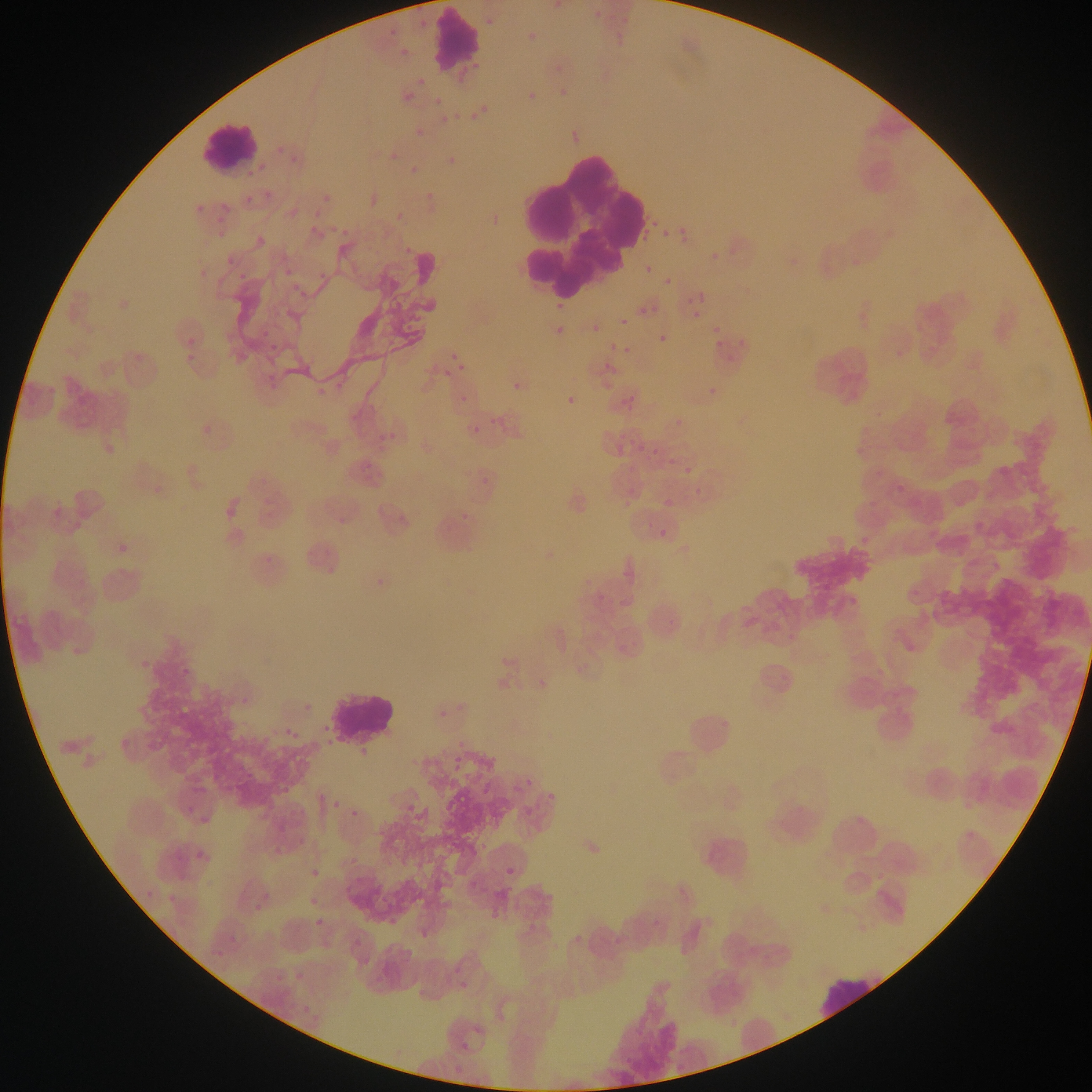

Approximate bounding boxes as [left, top, right, bottom] in pixels.
Summary:
  - Leukocyte locations: [436, 12, 479, 67], [201, 125, 258, 171], [514, 153, 644, 291], [321, 686, 400, 750], [818, 971, 889, 1016]
  - Plasmodium parasite locations (subset; some below the resolvable size): [410, 15, 429, 27], [485, 18, 493, 26], [384, 29, 392, 38], [395, 42, 410, 56], [452, 68, 473, 87], [416, 73, 427, 90], [399, 91, 418, 106], [471, 93, 489, 119], [434, 96, 443, 106], [435, 110, 460, 126], [383, 149, 400, 167], [287, 150, 302, 164], [441, 150, 466, 164], [409, 158, 423, 179], [268, 183, 289, 199], [202, 186, 226, 218], [359, 189, 378, 208], [242, 190, 258, 209], [424, 192, 440, 204], [288, 198, 309, 217], [394, 205, 410, 221], [644, 209, 660, 241], [304, 219, 318, 238], [331, 220, 352, 237], [681, 225, 694, 244], [260, 227, 273, 238], [319, 253, 339, 279], [224, 255, 237, 265], [645, 265, 653, 274], [236, 267, 257, 287], [284, 278, 307, 306], [663, 278, 671, 287], [682, 292, 704, 307], [550, 299, 570, 315], [648, 306, 665, 312], [638, 307, 647, 315], [693, 311, 701, 319], [620, 318, 628, 326], [551, 321, 571, 334], [587, 323, 601, 338], [253, 326, 282, 349], [713, 326, 721, 333], [658, 334, 667, 342], [187, 336, 196, 346], [605, 338, 622, 355], [445, 347, 474, 378], [604, 363, 612, 372], [444, 369, 452, 377], [510, 383, 524, 391], [563, 390, 580, 404], [614, 391, 638, 408], [457, 393, 467, 402], [487, 406, 501, 431], [196, 414, 217, 440], [102, 421, 130, 455], [470, 425, 480, 434], [625, 441, 635, 451], [638, 444, 644, 461], [652, 448, 660, 456], [667, 459, 676, 467], [685, 467, 693, 474], [481, 477, 489, 485], [895, 484, 906, 494], [664, 498, 674, 507], [623, 499, 631, 508], [219, 506, 246, 520], [337, 517, 346, 526], [974, 521, 983, 530], [658, 528, 666, 536], [855, 530, 871, 544], [110, 540, 132, 557], [993, 562, 1001, 571], [374, 579, 388, 586], [134, 651, 149, 670], [180, 653, 193, 676], [532, 678, 544, 690], [236, 687, 252, 707], [282, 709, 305, 740], [437, 710, 451, 722], [1041, 714, 1049, 722], [447, 747, 468, 777], [522, 772, 534, 786], [192, 775, 211, 799], [970, 775, 978, 784], [475, 781, 492, 799], [544, 781, 560, 811], [312, 786, 331, 803], [180, 793, 196, 815], [327, 795, 344, 814], [195, 799, 218, 826], [516, 801, 538, 817], [348, 806, 367, 820], [966, 831, 974, 840], [583, 841, 602, 858], [188, 850, 214, 865], [306, 866, 321, 878], [506, 867, 515, 876], [140, 886, 153, 900], [164, 886, 187, 925], [310, 899, 318, 907], [244, 901, 266, 919], [315, 919, 324, 927], [226, 930, 247, 949], [210, 944, 222, 958], [289, 965, 303, 982], [342, 972, 363, 996], [272, 977, 277, 985], [455, 977, 472, 1000], [296, 1005, 313, 1019], [461, 1042, 469, 1053] | approximate [x, y] pixel centers of objects too small to bound: [422, 137], [666, 234], [719, 344], [712, 390]
  - Country: Ghana
  - Image size: 1092×1092 pixels
  - Capture: mobile-phone photograph through a microscope
  - Field of view: single
  - Preparation: thin blood film